Report the malaria status of this cell.
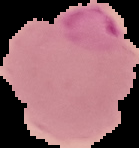

Parasitized.

image size = 139×148 pixels
image type = segmented cell region with the area outside set to black
preparation = thin blood film